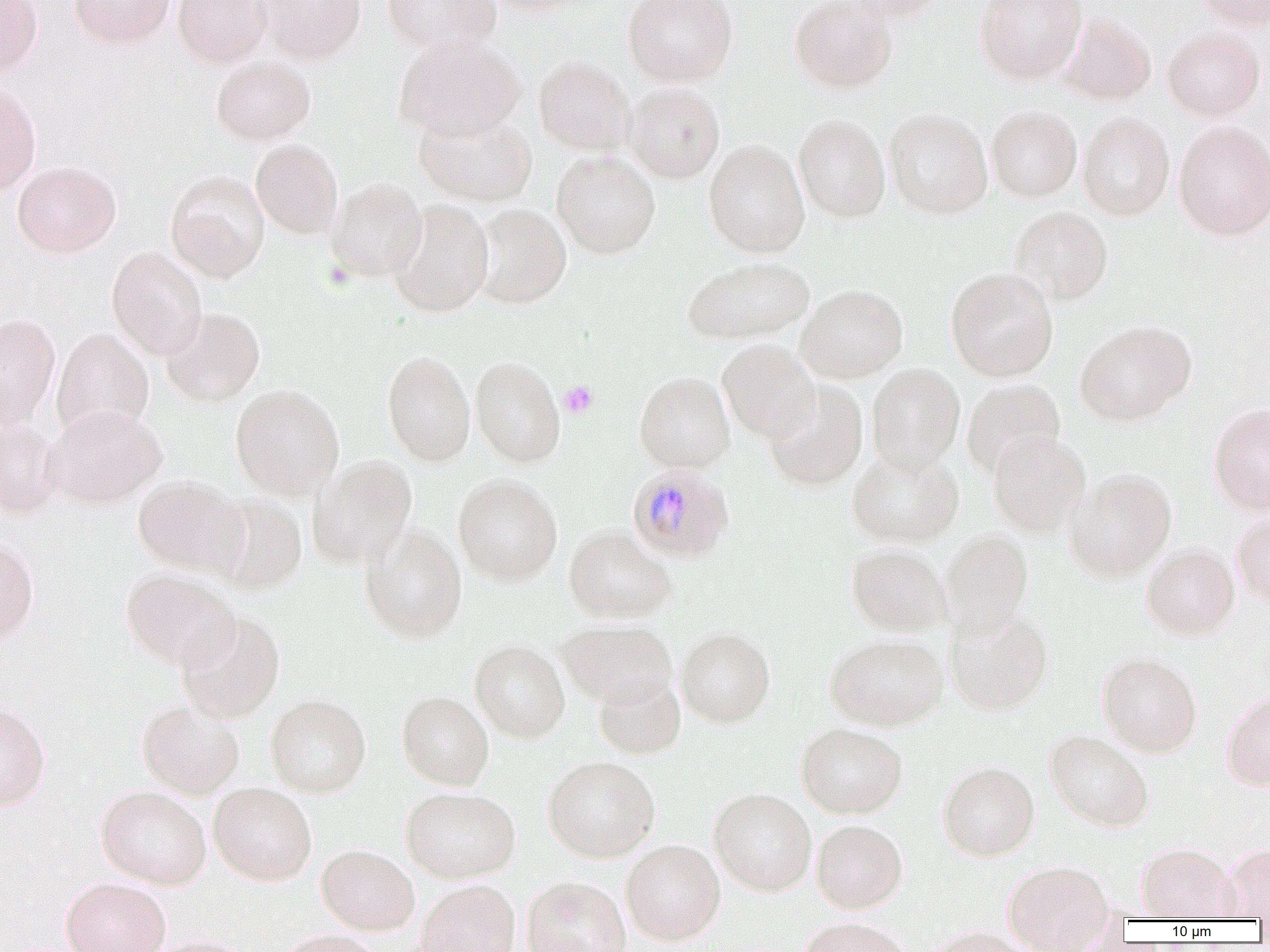
Approximate bounding boxes as named x1/y1/x2/y2 corners in pixels. Plasmodium malariae-infected red blood cell locations: (x1=626, y1=464, x2=734, y2=564). Platelet locations: (x1=559, y1=380, x2=599, y2=418). Uninfected red blood cell locations: (x1=0, y1=0, x2=43, y2=77), (x1=69, y1=0, x2=175, y2=50), (x1=172, y1=0, x2=271, y2=68), (x1=256, y1=0, x2=367, y2=65), (x1=382, y1=0, x2=501, y2=58), (x1=477, y1=0, x2=589, y2=15), (x1=623, y1=0, x2=737, y2=87), (x1=790, y1=0, x2=898, y2=94), (x1=839, y1=0, x2=950, y2=23), (x1=975, y1=0, x2=1087, y2=85), (x1=1193, y1=0, x2=1270, y2=31), (x1=1058, y1=13, x2=1156, y2=105), (x1=1162, y1=26, x2=1266, y2=122), (x1=393, y1=34, x2=525, y2=142), (x1=211, y1=56, x2=316, y2=145), (x1=534, y1=56, x2=634, y2=155), (x1=623, y1=81, x2=725, y2=183), (x1=0, y1=82, x2=42, y2=196), (x1=987, y1=105, x2=1082, y2=201), (x1=413, y1=108, x2=536, y2=207), (x1=884, y1=108, x2=993, y2=219), (x1=1077, y1=112, x2=1175, y2=221), (x1=793, y1=113, x2=890, y2=223), (x1=1173, y1=120, x2=1270, y2=240), (x1=250, y1=139, x2=343, y2=239), (x1=703, y1=140, x2=810, y2=258), (x1=551, y1=150, x2=660, y2=259), (x1=12, y1=160, x2=121, y2=258), (x1=166, y1=171, x2=270, y2=283), (x1=326, y1=177, x2=427, y2=283), (x1=388, y1=200, x2=494, y2=318), (x1=471, y1=203, x2=571, y2=309), (x1=1010, y1=206, x2=1113, y2=306), (x1=107, y1=247, x2=207, y2=360), (x1=681, y1=255, x2=814, y2=345), (x1=946, y1=267, x2=1059, y2=382), (x1=796, y1=283, x2=909, y2=383), (x1=161, y1=307, x2=265, y2=407), (x1=0, y1=313, x2=61, y2=428), (x1=1075, y1=320, x2=1196, y2=426), (x1=51, y1=327, x2=154, y2=441), (x1=717, y1=339, x2=820, y2=443), (x1=382, y1=349, x2=476, y2=467), (x1=470, y1=355, x2=566, y2=467), (x1=866, y1=362, x2=965, y2=474), (x1=634, y1=371, x2=735, y2=473), (x1=961, y1=378, x2=1065, y2=479), (x1=762, y1=382, x2=869, y2=492), (x1=230, y1=383, x2=344, y2=500), (x1=1208, y1=402, x2=1270, y2=514), (x1=45, y1=404, x2=166, y2=509), (x1=0, y1=418, x2=65, y2=519), (x1=988, y1=430, x2=1091, y2=537), (x1=846, y1=446, x2=964, y2=548), (x1=308, y1=454, x2=418, y2=570), (x1=1066, y1=467, x2=1177, y2=582), (x1=453, y1=473, x2=563, y2=587), (x1=133, y1=474, x2=248, y2=579), (x1=211, y1=491, x2=307, y2=595), (x1=1231, y1=513, x2=1270, y2=608), (x1=358, y1=521, x2=467, y2=643), (x1=563, y1=524, x2=677, y2=623), (x1=939, y1=529, x2=1034, y2=637), (x1=0, y1=537, x2=40, y2=646), (x1=847, y1=544, x2=950, y2=637), (x1=1141, y1=544, x2=1239, y2=640), (x1=120, y1=569, x2=239, y2=672), (x1=944, y1=606, x2=1054, y2=716), (x1=176, y1=611, x2=285, y2=723), (x1=557, y1=620, x2=677, y2=709), (x1=676, y1=626, x2=776, y2=728), (x1=825, y1=634, x2=948, y2=731), (x1=469, y1=639, x2=570, y2=743), (x1=1097, y1=651, x2=1202, y2=756), (x1=594, y1=674, x2=685, y2=759), (x1=397, y1=690, x2=494, y2=790), (x1=1221, y1=691, x2=1270, y2=790), (x1=266, y1=693, x2=371, y2=797), (x1=137, y1=700, x2=244, y2=799), (x1=0, y1=701, x2=51, y2=812), (x1=795, y1=723, x2=908, y2=819), (x1=1044, y1=729, x2=1154, y2=831), (x1=543, y1=755, x2=661, y2=862), (x1=938, y1=761, x2=1040, y2=861), (x1=208, y1=781, x2=317, y2=885), (x1=97, y1=785, x2=211, y2=889), (x1=400, y1=786, x2=520, y2=883), (x1=709, y1=787, x2=817, y2=896), (x1=811, y1=819, x2=908, y2=913), (x1=620, y1=838, x2=726, y2=945), (x1=1137, y1=842, x2=1238, y2=921), (x1=1222, y1=842, x2=1270, y2=920), (x1=316, y1=844, x2=420, y2=935), (x1=1002, y1=859, x2=1114, y2=950), (x1=521, y1=875, x2=631, y2=952), (x1=61, y1=876, x2=171, y2=952), (x1=416, y1=878, x2=521, y2=952), (x1=797, y1=918, x2=913, y2=952), (x1=924, y1=926, x2=1040, y2=952), (x1=276, y1=928, x2=388, y2=952), (x1=143, y1=934, x2=260, y2=952). Slide-level diagnosis: Plasmodium malariae. Image is 1270×952 pixels. Thin blood film. Light microscopy. Single field of view. Captured at 1000x magnification.